Identify the preparation type.
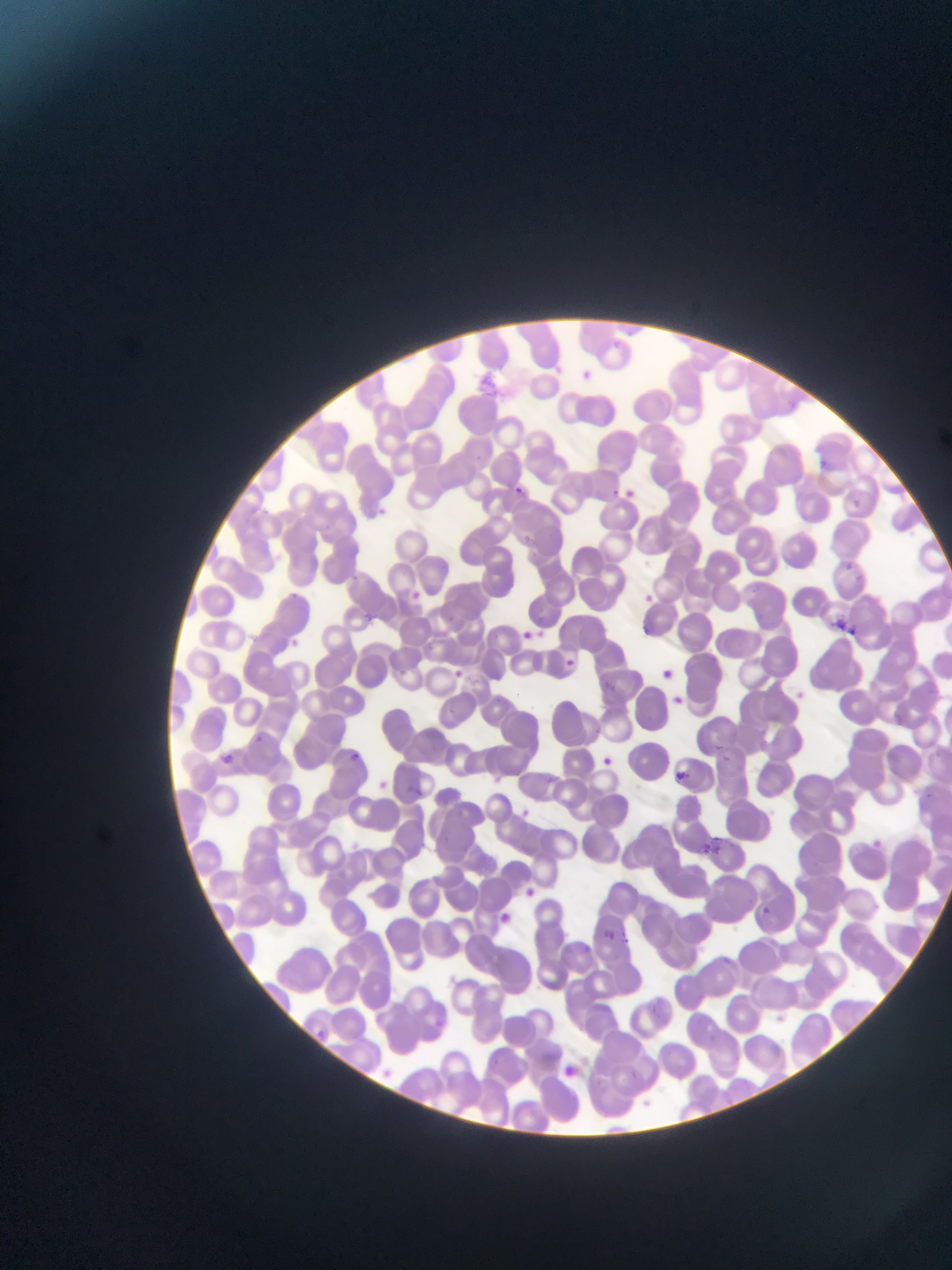
Thin blood film.

Approximate bounding boxes as left top right bottom in pixels.
Summary:
  - Plasmodium parasite locations: 609 338 620 348; 584 368 595 377; 819 460 827 469; 509 483 527 499; 608 486 633 508; 617 487 637 505; 379 506 396 519; 836 558 858 576; 406 588 423 603; 637 590 658 609; 361 612 378 627; 831 619 855 637; 843 623 857 637; 641 624 652 636; 516 627 537 644; 284 635 302 652; 559 655 578 672; 658 666 677 683; 450 668 466 681; 792 688 807 703; 669 695 686 710; 250 732 267 747; 711 744 732 762; 348 749 358 761; 217 750 238 769; 600 754 616 768; 674 769 690 784; 372 778 391 795; 518 806 533 819; 871 837 885 850; 864 839 883 856; 523 886 539 901; 760 905 773 918; 493 910 510 927; 602 928 619 945; 623 935 637 944; 583 940 589 954; 311 1026 330 1044; 558 1064 578 1082; 627 1068 643 1082; 640 1097 654 1110
  - Capture: mobile-phone photograph through a microscope
  - Country: Ghana
  - Image size: 952×1270 pixels
  - Field of view: single